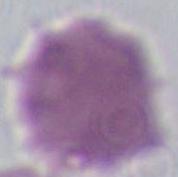 Captured at 1000x magnification. An erythrocyte is seen. Micrograph.